Identify the parasite.
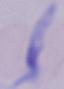

This is a trypanosome.

Micrograph. Captured at 1000x magnification.